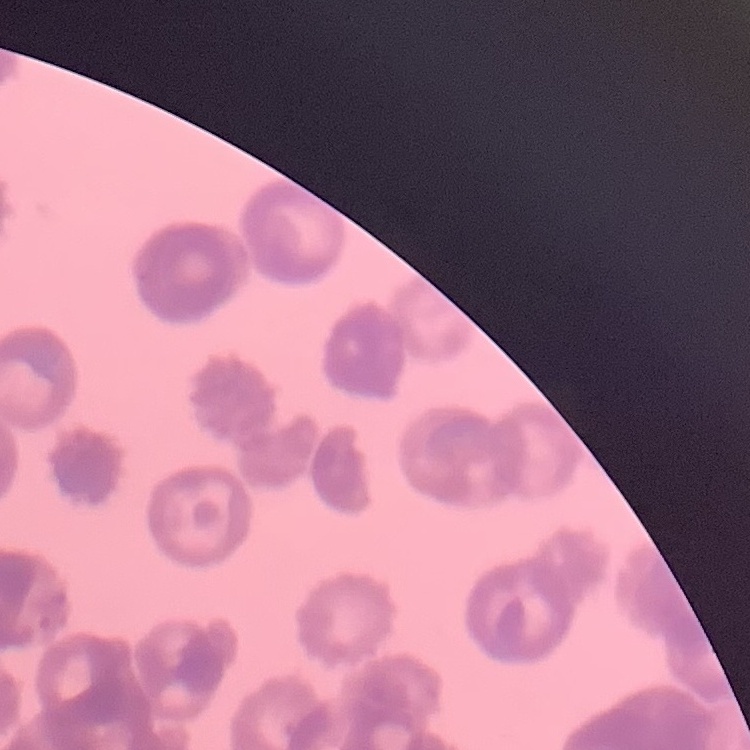 The erythrocytes show rouleaux formation. Stained with either Field's or Giemsa. Thin blood smear. Square crop of a larger photomicrograph.